Classify this cell by malaria status.
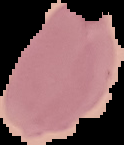

It is uninfected.

{
  "image_type": "cell region segmented out of the field of view; surrounding area masked to black",
  "preparation": "thin blood smear",
  "image_size": "124×145 pixels"
}